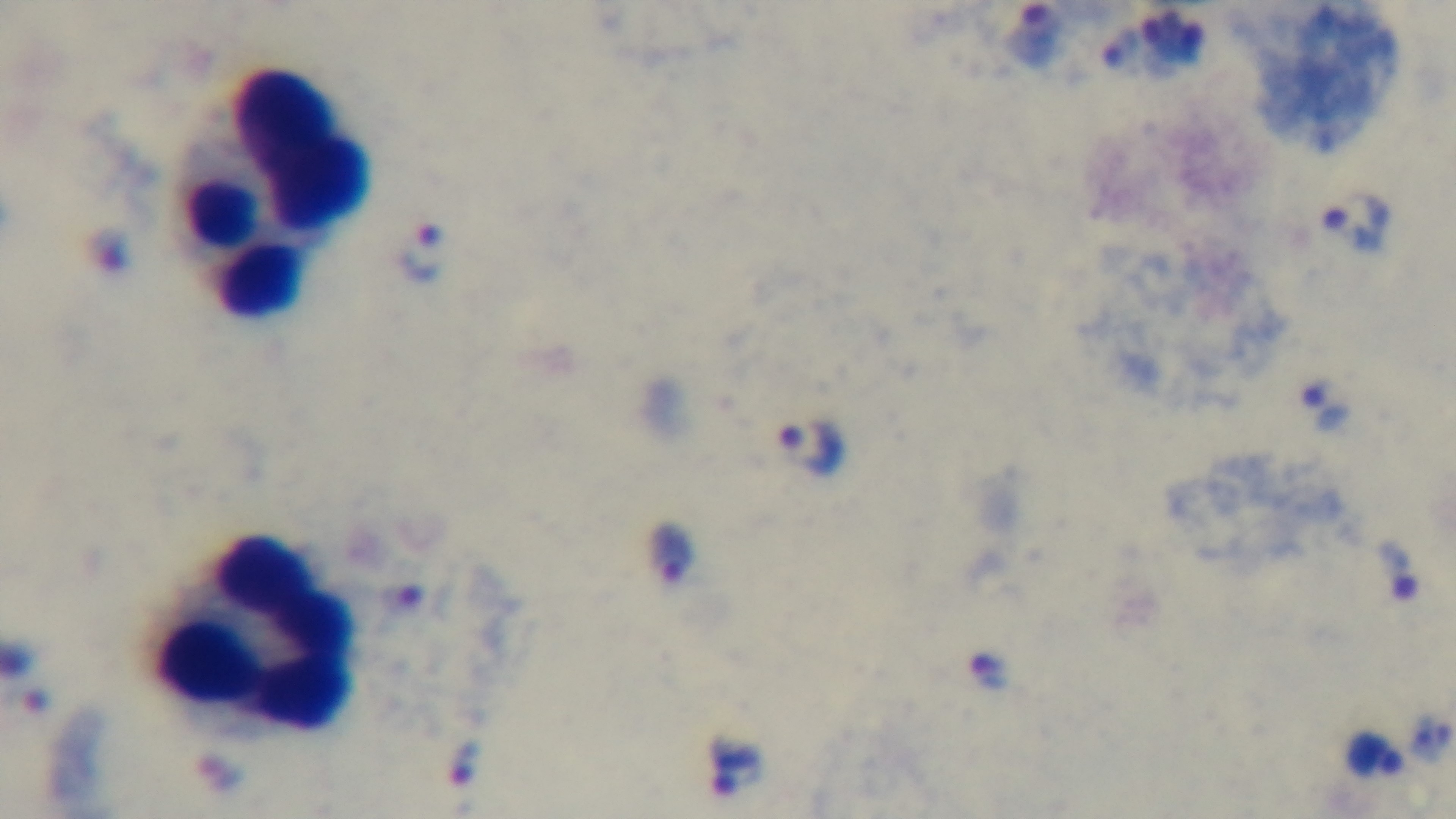
malaria status = infected
preparation = thick smear
field of view = single
objective = 100x oil immersion
stain = Giemsa
capture = mounted 4K digital camera
modality = light microscopy